Describe the morphology of the red blood cells.
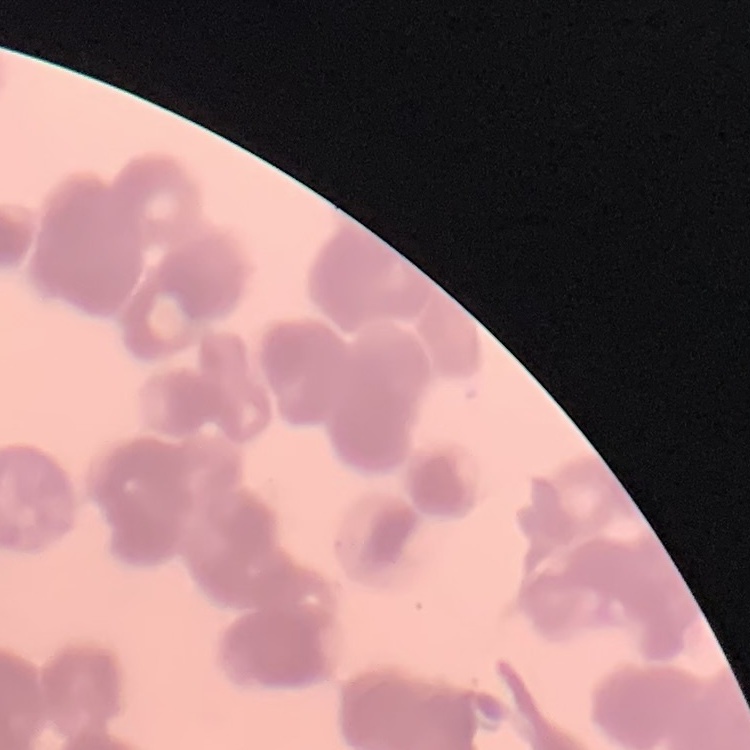
They show rouleaux formation.

Summary:
  - Stain: Field's or Giemsa
  - Image type: one tile cut from a larger photomicrograph
  - Preparation: thin blood smear